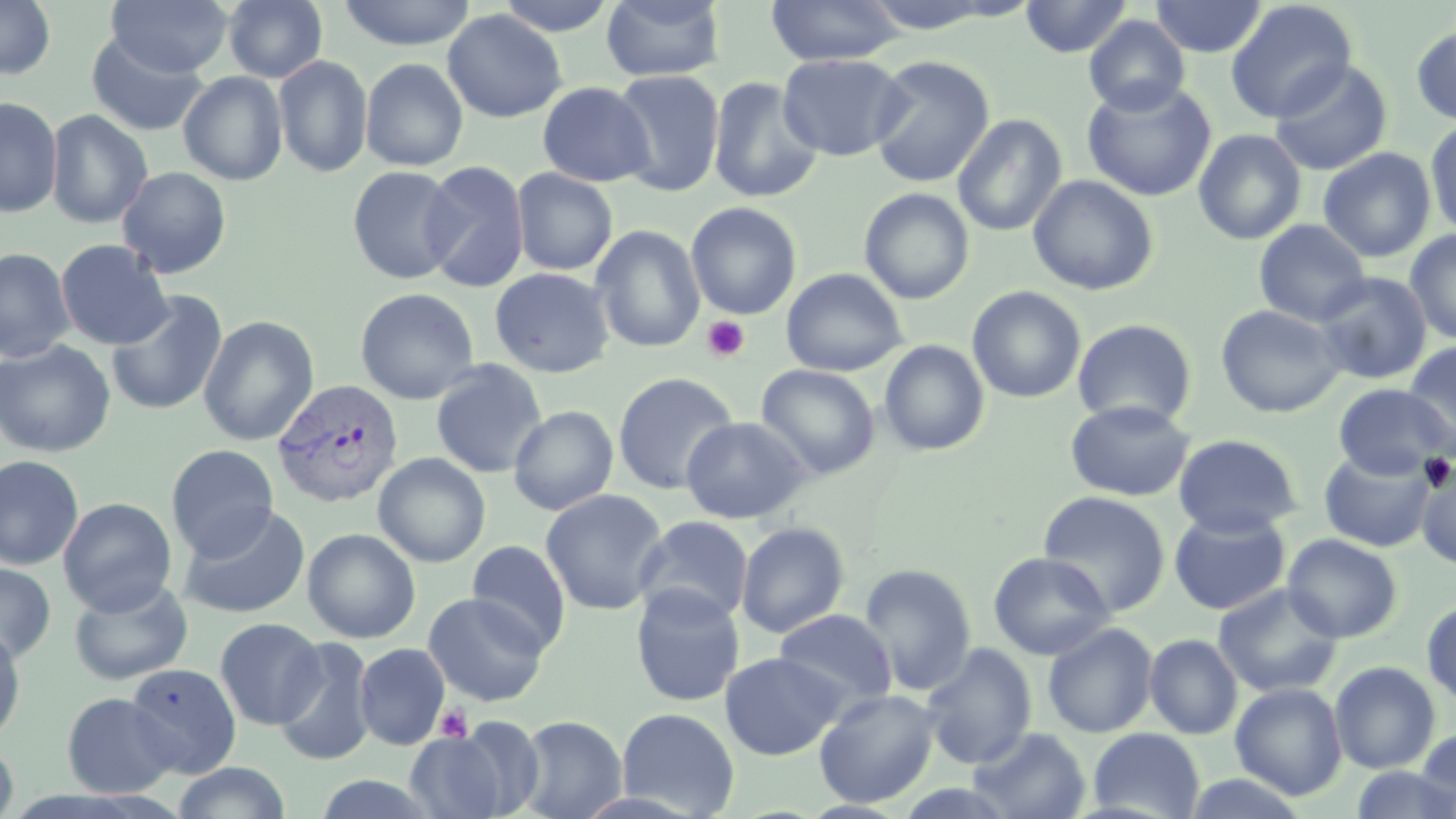
Approximate bounding boxes as (x1,y1)-(x2,y2) corner pairs in pixels. Platelet locations: (702,315)-(750,362), (435,705)-(472,743). Plasmodium vivax-infected red blood cell locations: (271,378)-(403,508). Uninfected red blood cell locations: (0,0)-(56,80), (106,0)-(233,78), (223,0)-(328,83), (337,0)-(477,50), (492,0)-(620,36), (600,0)-(727,82), (765,0)-(906,66), (1020,0)-(1133,58), (1149,0)-(1268,58), (1224,1)-(1357,123), (442,9)-(567,123), (1083,15)-(1190,116), (1411,20)-(1456,126), (86,32)-(209,137), (777,53)-(909,161), (273,55)-(373,177), (868,55)-(994,187), (360,58)-(469,171), (1268,59)-(1393,176), (611,69)-(725,197), (178,71)-(288,186), (707,76)-(823,204), (1081,80)-(1216,201), (537,81)-(655,186), (0,97)-(62,217), (45,109)-(153,229), (951,114)-(1067,237), (1425,118)-(1456,239), (1193,129)-(1307,245), (1317,147)-(1436,262), (419,159)-(530,292), (346,165)-(462,284), (116,166)-(232,279), (511,168)-(618,275), (1028,174)-(1159,296), (858,188)-(974,304), (685,201)-(802,320), (1254,219)-(1372,326), (591,224)-(706,353), (1404,229)-(1456,345), (55,239)-(173,350), (0,247)-(75,363), (488,267)-(616,378), (780,268)-(908,376), (1313,272)-(1432,384), (967,286)-(1086,403), (355,287)-(480,405), (106,290)-(228,416), (1215,303)-(1347,418), (198,315)-(319,446), (1072,318)-(1198,429), (0,340)-(116,457), (879,340)-(989,456), (1402,341)-(1456,456), (430,360)-(548,479), (756,364)-(880,480), (612,371)-(739,494), (1333,383)-(1454,480), (1065,399)-(1194,501), (508,405)-(619,515), (680,416)-(811,523), (1173,433)-(1303,537), (165,444)-(279,560), (1316,450)-(1435,553), (373,452)-(491,567), (0,455)-(84,571), (1417,465)-(1456,571), (540,490)-(668,615), (1038,491)-(1170,616), (58,497)-(177,616), (178,502)-(311,620), (1169,510)-(1291,616), (634,515)-(754,626), (736,521)-(850,638), (302,527)-(421,643), (1282,534)-(1402,642), (466,540)-(571,654), (988,552)-(1115,660), (0,561)-(56,664), (859,563)-(977,695), (68,577)-(193,685), (1213,583)-(1343,697), (630,584)-(745,707), (423,591)-(549,706), (1422,598)-(1456,706), (772,608)-(897,710), (214,617)-(326,729), (1042,622)-(1158,738), (0,623)-(26,743), (1145,633)-(1242,739), (273,637)-(376,765), (354,642)-(450,750), (920,643)-(1037,768), (720,652)-(846,760), (1329,661)-(1440,773), (125,662)-(241,778), (1230,683)-(1347,800), (814,689)-(940,808), (61,692)-(178,798), (616,707)-(740,818), (516,715)-(627,819), (441,717)-(548,817), (967,726)-(1092,819), (1088,727)-(1206,819), (1416,727)-(1456,817), (404,730)-(512,819), (0,739)-(19,819), (171,762)-(291,819), (1348,767)-(1456,819), (1177,772)-(1312,817), (309,773)-(443,818). Slide-level diagnosis: Plasmodium vivax. Thin blood film. Single field of view. May-Grünwald-Giemsa stain. 1000x magnification. Image is 1456×819 pixels. Light microscopy.